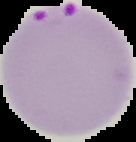
result: Plasmodium parasites detected
image_type: cell region segmented out of the field of view; surrounding area masked to black
image_size: 136×142 pixels
preparation: thin blood smear